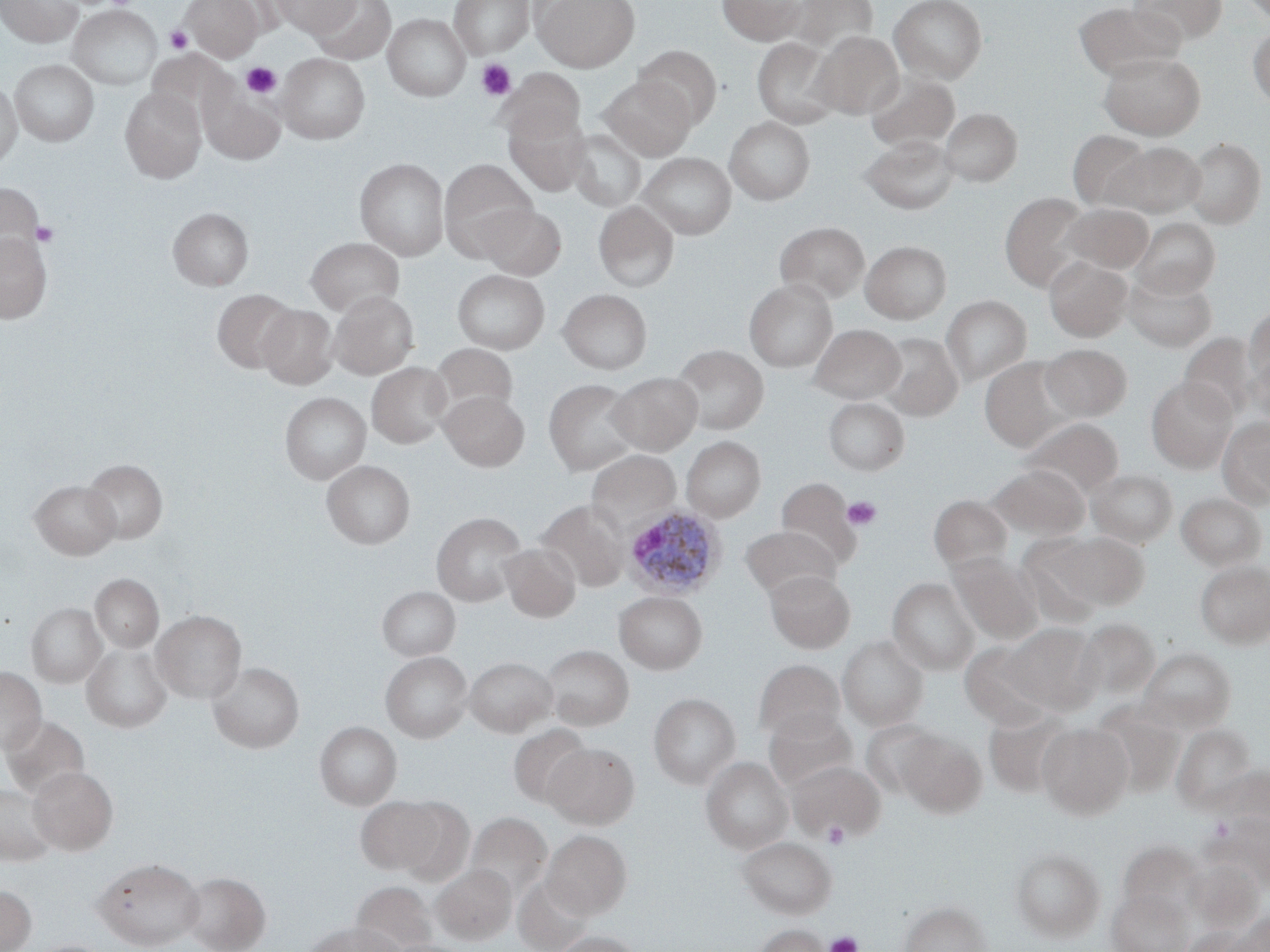 Approximate bounding boxes as [x1, y1, x2, y2] in pixels. Uninfected red blood cell locations: [1, 0, 82, 47], [181, 0, 264, 61], [273, 0, 360, 36], [311, 0, 396, 64], [449, 0, 533, 58], [533, 0, 638, 72], [718, 0, 806, 45], [787, 0, 878, 54], [889, 0, 987, 83], [1130, 0, 1228, 44], [1239, 0, 1270, 22], [1073, 2, 1185, 80], [68, 6, 162, 89], [383, 14, 470, 101], [1247, 27, 1270, 106], [813, 31, 903, 118], [752, 37, 841, 128], [634, 45, 721, 127], [147, 49, 230, 123], [1099, 52, 1205, 139], [277, 53, 370, 144], [10, 60, 99, 146], [497, 68, 585, 144], [866, 72, 959, 153], [599, 76, 695, 160], [0, 78, 22, 169], [120, 88, 207, 182], [201, 88, 285, 163], [504, 108, 591, 196], [940, 108, 1022, 186], [724, 117, 814, 204], [567, 128, 647, 212], [1067, 131, 1151, 210], [860, 134, 958, 214], [1184, 137, 1266, 228], [1106, 142, 1205, 217], [638, 152, 737, 239], [354, 158, 449, 260], [439, 159, 537, 256], [1, 182, 43, 263], [1000, 192, 1093, 291], [594, 201, 679, 292], [478, 203, 566, 280], [1063, 204, 1153, 273], [168, 207, 253, 290], [1132, 217, 1220, 297], [775, 222, 869, 304], [0, 232, 52, 322], [305, 237, 405, 315], [861, 241, 952, 324], [1044, 256, 1132, 341], [452, 270, 550, 354], [1124, 272, 1217, 352], [744, 280, 837, 372], [212, 288, 298, 372], [557, 289, 652, 374], [329, 291, 419, 378], [941, 295, 1031, 386], [257, 304, 338, 389], [1244, 307, 1270, 390], [811, 324, 905, 403], [876, 333, 963, 420], [1179, 334, 1258, 421], [429, 344, 517, 423], [1040, 344, 1132, 421], [672, 346, 769, 434], [1246, 355, 1270, 428], [979, 358, 1074, 451], [367, 363, 452, 448], [608, 372, 702, 455], [1146, 377, 1237, 472], [544, 378, 640, 475], [440, 391, 529, 471], [279, 392, 370, 484], [824, 397, 909, 476], [1218, 417, 1270, 507], [1022, 418, 1124, 499], [682, 437, 766, 521], [586, 450, 681, 533], [82, 459, 168, 544], [322, 461, 414, 548], [989, 464, 1090, 540], [1087, 469, 1178, 546], [776, 477, 861, 568], [30, 480, 120, 559], [1176, 493, 1266, 570], [929, 494, 1012, 572], [539, 501, 628, 592], [432, 512, 526, 606], [740, 525, 840, 600], [1054, 532, 1149, 610], [500, 543, 580, 622], [949, 553, 1043, 643], [1195, 560, 1270, 648], [765, 570, 855, 652], [90, 574, 163, 652], [888, 578, 979, 674], [378, 586, 460, 660], [614, 591, 707, 673], [26, 603, 107, 687], [152, 610, 246, 703], [1074, 619, 1160, 701], [1002, 623, 1100, 713], [838, 636, 928, 730], [960, 642, 1055, 729], [82, 644, 172, 732], [542, 645, 633, 730], [1139, 647, 1236, 732], [380, 651, 472, 742], [465, 656, 557, 736], [754, 660, 845, 742], [208, 662, 304, 753], [0, 668, 46, 753], [649, 693, 740, 788], [1092, 701, 1184, 795], [765, 709, 857, 790], [983, 709, 1073, 798], [1, 715, 90, 800], [315, 721, 401, 809], [861, 721, 940, 796], [1037, 722, 1133, 818], [508, 724, 591, 807], [1171, 724, 1257, 812], [895, 730, 986, 816], [543, 743, 638, 828], [702, 758, 793, 853], [789, 760, 884, 840], [28, 766, 118, 854], [0, 784, 57, 865], [355, 795, 444, 875], [392, 797, 475, 886], [1217, 812, 1270, 888], [466, 813, 552, 899], [542, 830, 631, 918], [737, 837, 836, 918], [1120, 841, 1207, 920], [1011, 847, 1104, 941], [94, 858, 204, 949], [432, 864, 516, 944], [181, 872, 270, 952], [513, 875, 595, 952], [351, 882, 437, 952], [0, 886, 36, 952], [1107, 888, 1192, 952], [899, 900, 991, 952], [1231, 913, 1270, 952], [308, 922, 399, 952], [752, 924, 829, 952], [1180, 927, 1257, 952], [551, 931, 642, 952]. Plasmodium ovale-infected red blood cell locations: [622, 506, 726, 601]. Platelet locations: [164, 26, 193, 54], [476, 59, 516, 101], [242, 61, 281, 99], [31, 221, 59, 247], [843, 496, 882, 531], [1208, 816, 1236, 842], [823, 822, 849, 848], [825, 932, 862, 952]. Slide-level diagnosis: Plasmodium ovale. Thin blood film. Single field of view. Image is 1270×952 pixels. Captured at 1000x magnification. Light microscopy. May-Grünwald-Giemsa-stained preparation.